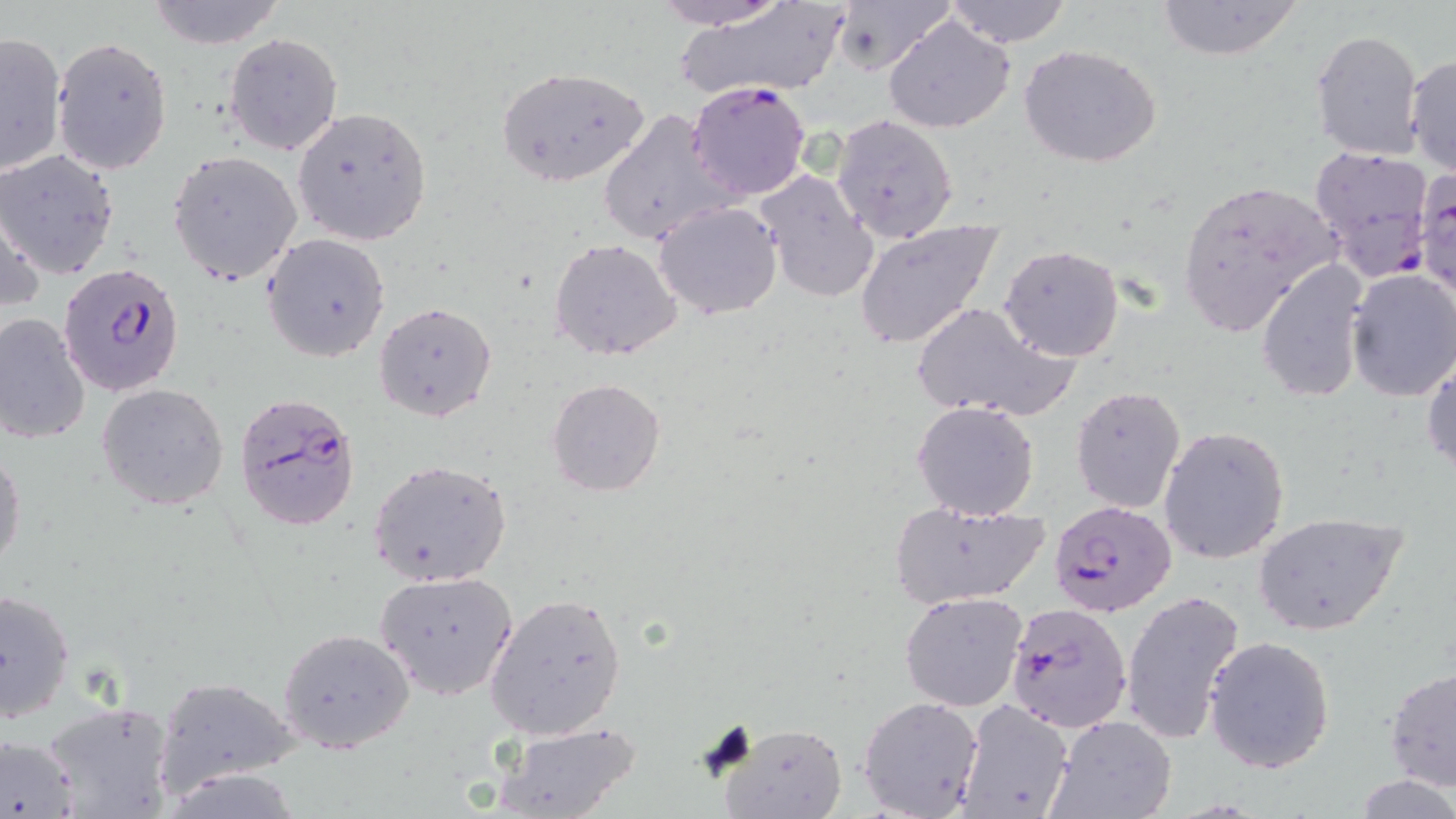 Approximate bounding boxes as [x1, y1, x2, y2] in pixels. Uninfected red blood cell locations: [147, 0, 285, 49], [649, 0, 791, 29], [830, 0, 954, 78], [943, 0, 1073, 48], [1154, 0, 1306, 63], [670, 2, 853, 105], [882, 14, 1017, 134], [1309, 29, 1426, 163], [0, 30, 67, 175], [225, 33, 342, 155], [53, 36, 172, 178], [1020, 44, 1165, 169], [1405, 52, 1456, 178], [496, 66, 648, 187], [291, 106, 432, 247], [599, 109, 733, 247], [830, 114, 960, 244], [0, 149, 122, 279], [169, 150, 303, 286], [1412, 167, 1456, 299], [753, 168, 879, 302], [1177, 177, 1340, 337], [0, 191, 46, 316], [653, 200, 783, 319], [854, 220, 1003, 351], [262, 232, 391, 363], [548, 237, 684, 362], [999, 243, 1125, 362], [1257, 256, 1371, 402], [1344, 270, 1456, 401], [374, 301, 498, 423], [913, 302, 1072, 421], [0, 311, 92, 445], [1423, 352, 1456, 477], [545, 378, 666, 497], [96, 383, 229, 509], [1070, 385, 1186, 513], [912, 399, 1041, 519], [1159, 424, 1292, 565], [0, 443, 25, 575], [368, 459, 513, 587], [887, 498, 1051, 609], [1253, 511, 1407, 636], [375, 570, 519, 700], [0, 587, 76, 725], [1121, 588, 1247, 744], [900, 590, 1028, 712], [484, 592, 628, 740], [278, 629, 414, 752], [1203, 636, 1335, 774], [1383, 666, 1456, 794], [152, 677, 302, 795], [858, 695, 984, 818], [955, 697, 1074, 819], [40, 701, 177, 819], [1048, 714, 1177, 819], [489, 722, 644, 819], [717, 724, 850, 819], [0, 733, 81, 819], [1354, 774, 1456, 818]. Plasmodium falciparum-infected red blood cell locations: [686, 80, 813, 202], [1309, 144, 1434, 280], [57, 263, 184, 395], [233, 391, 363, 532], [1050, 503, 1180, 618], [1005, 601, 1135, 734]. Slide-level diagnosis: Plasmodium falciparum. Image is 1456×819 pixels. Thin blood smear. Light microscopy. May-Grünwald-Giemsa stain. 1000x magnification. One field of a larger specimen.